Name the blood parasite species.
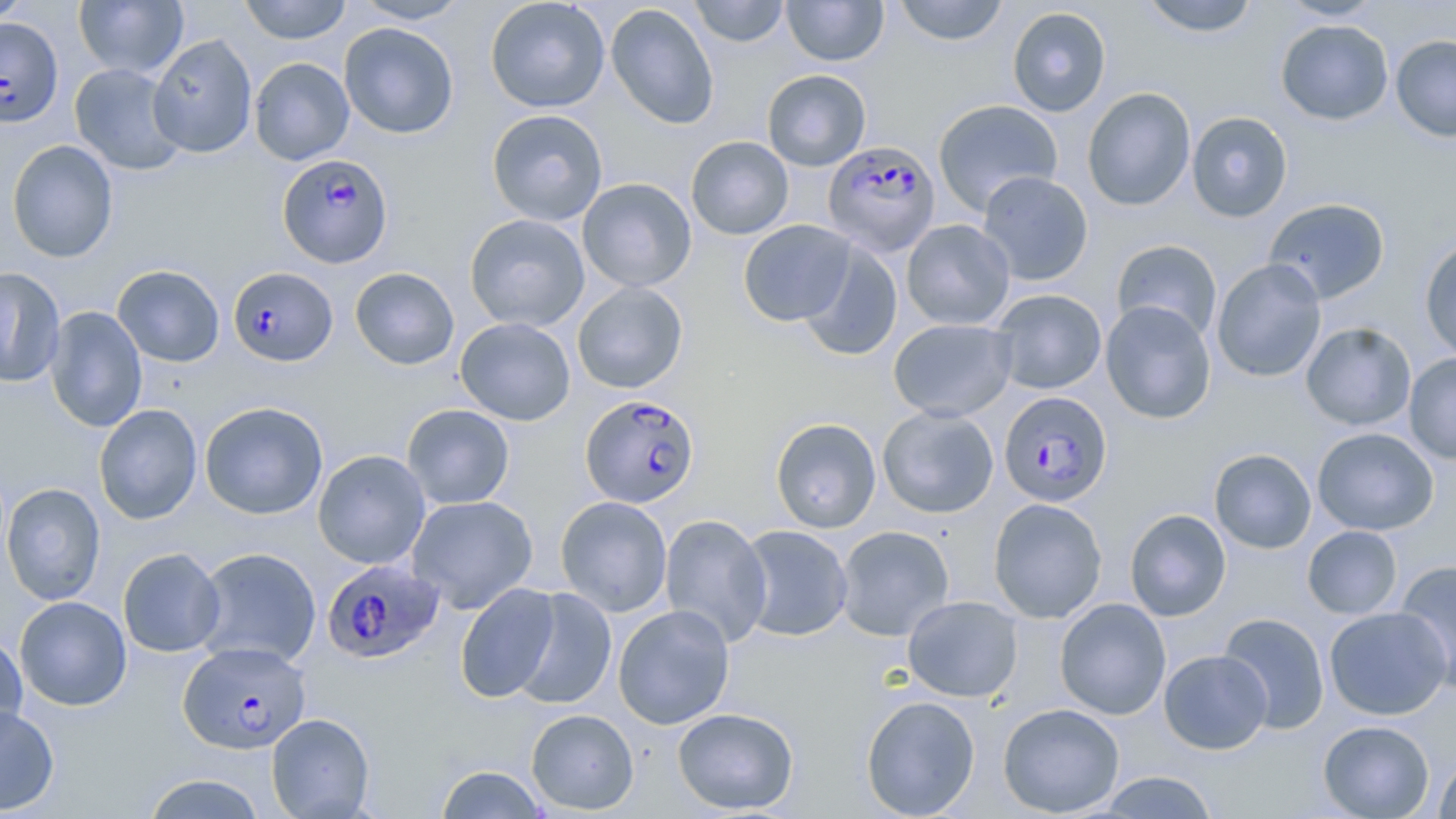
Plasmodium falciparum.

Summary:
  - Coordinate format: approximate bounding boxes as (x1, y1, x2, y2) in pixels
  - Uninfected red blood cell locations: (0, 0, 35, 24), (74, 0, 188, 79), (239, 0, 351, 44), (351, 0, 471, 24), (485, 0, 610, 113), (689, 0, 790, 47), (781, 0, 889, 66), (893, 0, 1009, 45), (1139, 0, 1260, 37), (1278, 0, 1387, 21), (606, 3, 719, 129), (1007, 7, 1111, 117), (1275, 19, 1393, 125), (339, 22, 459, 139), (147, 33, 258, 158), (1391, 34, 1456, 143), (249, 57, 354, 165), (69, 63, 187, 175), (762, 69, 871, 171), (1082, 86, 1196, 211), (932, 99, 1063, 216), (486, 108, 608, 226), (1186, 111, 1293, 222), (686, 136, 794, 240), (7, 140, 119, 263), (977, 171, 1093, 286), (577, 178, 697, 292), (1263, 197, 1391, 304), (464, 213, 590, 332), (738, 219, 856, 326), (901, 219, 1015, 330), (1419, 238, 1456, 363), (1111, 239, 1223, 343), (797, 241, 903, 361), (1211, 259, 1326, 382), (112, 264, 225, 367), (0, 267, 66, 389), (349, 267, 459, 370), (572, 282, 688, 393), (990, 288, 1107, 395), (1101, 300, 1217, 424), (44, 305, 148, 432), (455, 317, 575, 426), (888, 318, 1016, 422), (1301, 322, 1416, 431), (1404, 353, 1456, 465), (200, 401, 328, 519), (93, 404, 203, 525), (402, 404, 515, 510), (877, 406, 999, 518), (770, 417, 882, 533), (1312, 427, 1439, 535), (1209, 448, 1316, 554), (312, 449, 431, 569), (1, 483, 105, 605), (406, 494, 538, 613), (555, 496, 673, 617), (988, 498, 1108, 624), (1124, 509, 1231, 621), (660, 514, 772, 646), (736, 525, 854, 642), (835, 525, 955, 641), (1302, 525, 1402, 620), (194, 547, 321, 668), (118, 548, 226, 657), (1393, 560, 1456, 692), (454, 583, 560, 704), (511, 588, 617, 711), (14, 595, 132, 711), (902, 596, 1024, 702), (1054, 597, 1171, 720), (613, 604, 735, 729), (1323, 606, 1452, 720), (1217, 612, 1330, 734), (0, 631, 28, 742), (1159, 649, 1272, 754), (860, 695, 980, 818), (998, 702, 1125, 817), (0, 705, 59, 815), (672, 707, 799, 815), (526, 709, 639, 815), (266, 713, 376, 818), (1318, 720, 1434, 818), (1433, 756, 1456, 818), (435, 765, 549, 818), (1096, 771, 1219, 818), (142, 773, 267, 818)
  - Plasmodium falciparum-infected red blood cell locations: (1, 21, 64, 129), (823, 140, 941, 257), (276, 153, 394, 268), (224, 270, 338, 365), (999, 392, 1114, 507), (581, 394, 700, 512), (321, 558, 444, 664), (178, 642, 311, 753)
  - Image size: 1456×819 pixels
  - Preparation: thin blood film
  - Field of view: one of a larger specimen
  - Magnification: 1000x
  - Stain: May-Grünwald-Giemsa
  - Modality: light microscopy